State which parasite is depicted.
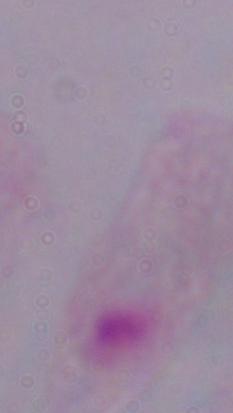
A trichomonad.

magnification = 1000x
modality = photomicrograph